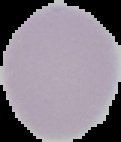 From a thin blood smear. Cell region segmented out of the field of view; the surrounding area is masked to black. Image is 121×142 pixels. Result: negative for Plasmodium parasites.